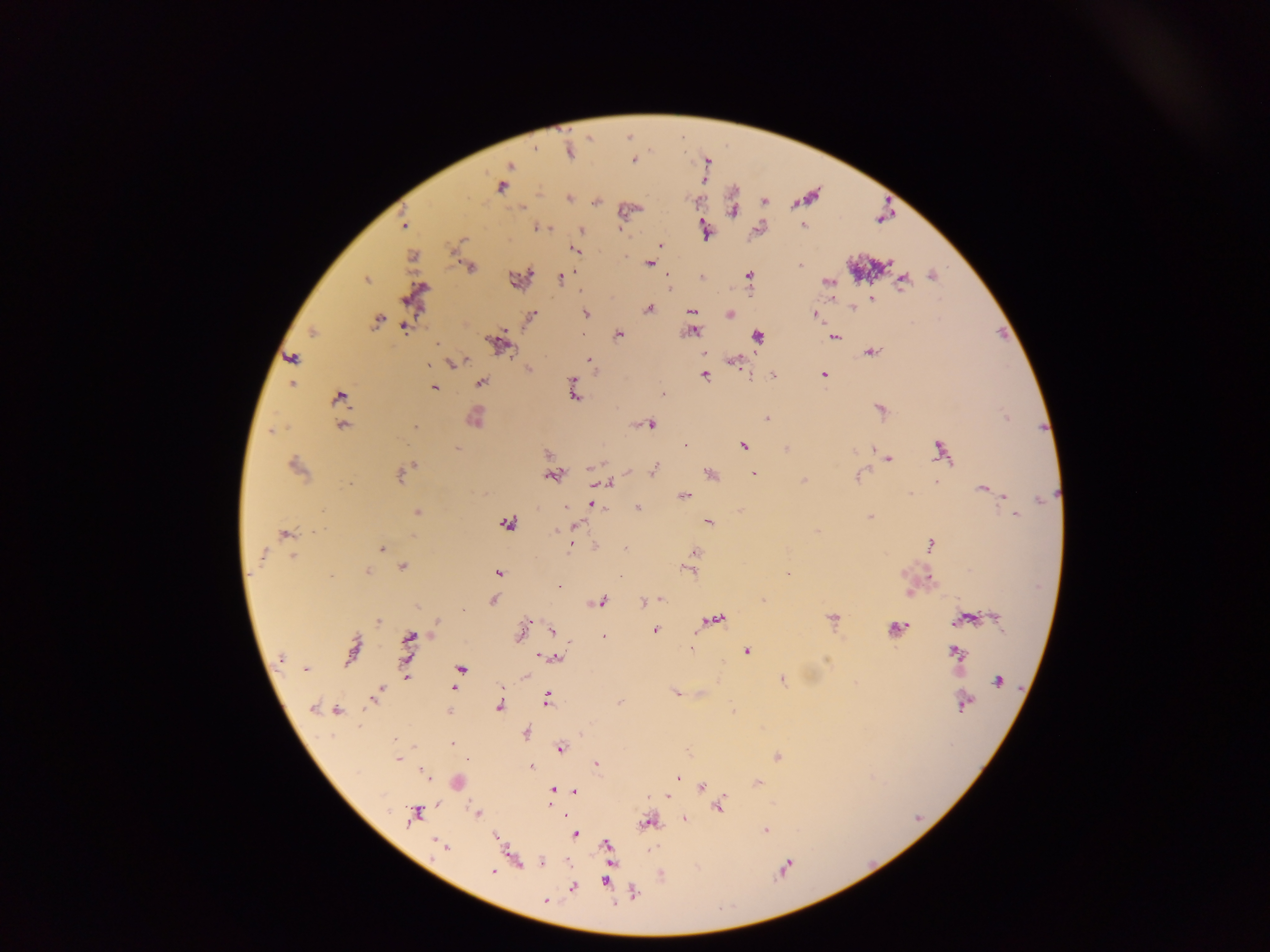
Plasmodium parasite locations = approximate centers as [x, y] in pixels: [569, 151], [634, 161], [510, 165], [501, 187], [569, 199], [764, 201], [596, 202], [523, 207], [732, 211], [803, 225], [403, 226], [541, 227], [581, 230], [660, 245], [574, 249], [411, 256], [650, 263], [799, 265], [471, 267], [749, 275], [932, 276], [668, 277], [701, 277], [366, 278], [561, 278], [903, 281], [829, 283], [415, 297], [871, 299], [853, 308], [649, 309], [692, 310], [585, 313], [730, 314], [815, 315], [531, 316], [377, 320], [405, 328], [313, 332], [693, 332], [582, 334], [619, 335], [758, 337], [835, 337], [498, 345], [704, 352], [872, 352], [292, 358], [589, 359], [733, 362], [454, 363], [529, 368], [823, 374], [772, 375], [705, 376], [292, 383], [481, 383], [574, 384], [434, 388], [575, 394], [663, 394], [340, 397], [881, 409], [475, 418], [768, 418], [651, 425], [342, 426], [415, 427], [684, 445], [743, 446], [457, 448], [941, 451], [547, 453], [888, 458], [296, 467], [411, 468], [654, 469], [402, 474], [710, 474], [754, 474], [552, 476], [859, 476], [805, 480], [936, 482], [607, 483], [982, 488], [910, 494], [684, 496], [1005, 496], [1040, 499], [593, 504], [566, 507], [637, 508], [417, 512], [1015, 515], [870, 517], [707, 522], [507, 523], [577, 525], [556, 531], [284, 533], [930, 544], [571, 546], [382, 548], [625, 548], [694, 553], [263, 556], [294, 556], [403, 567], [367, 572], [689, 572], [497, 573], [787, 573], [332, 576], [620, 577], [559, 586], [661, 599], [493, 601], [656, 601], [601, 602], [644, 603], [997, 617], [715, 619], [832, 619], [964, 619], [378, 621], [527, 621], [438, 623], [896, 628], [655, 630], [553, 631], [519, 636], [603, 637], [408, 641], [691, 648], [352, 650], [407, 651], [747, 651], [955, 653], [541, 657], [555, 657], [280, 658], [305, 668], [461, 668], [525, 676], [407, 677], [782, 680], [997, 681], [455, 688], [379, 693], [675, 693], [548, 699], [620, 702], [964, 704], [499, 706], [312, 707], [337, 711], [448, 712], [525, 732], [395, 739], [453, 744], [561, 748], [777, 757], [399, 759], [596, 763], [532, 767], [424, 774], [677, 778], [757, 783], [702, 786], [552, 791], [575, 791], [667, 796], [720, 806], [477, 813], [414, 814], [685, 818], [647, 822], [765, 830], [575, 834], [496, 837], [439, 844], [606, 845], [445, 846], [543, 863], [784, 868], [493, 872], [605, 881], [573, 887], [633, 892], [546, 901]
country = Ghana
image size = 1270×952 pixels
preparation = thick blood film
capture = mobile-phone photograph through a microscope
field of view = single